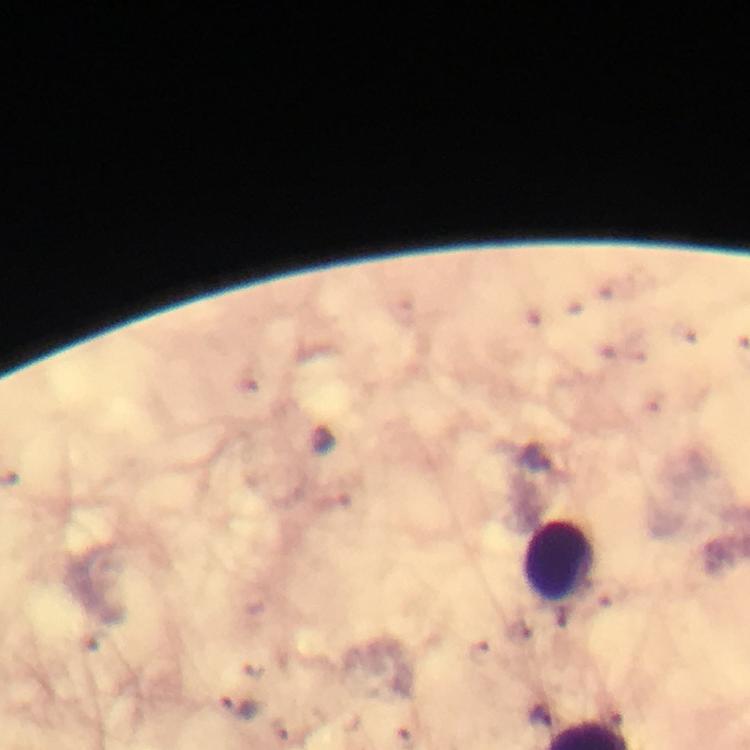

leukocyte locations = approximate centers as {x, y} in pixels: {558, 561}
immersion oil = used
malaria parasite locations = approximate centers as {x, y} in pixels: {536, 458}, {239, 706}
cropped from = one field of view
context = from a malaria diagnostic workup
preparation = thick blood smear
image size = 750×750 pixels
capture = smartphone camera through the microscope
magnification = 100x
stain = Giemsa